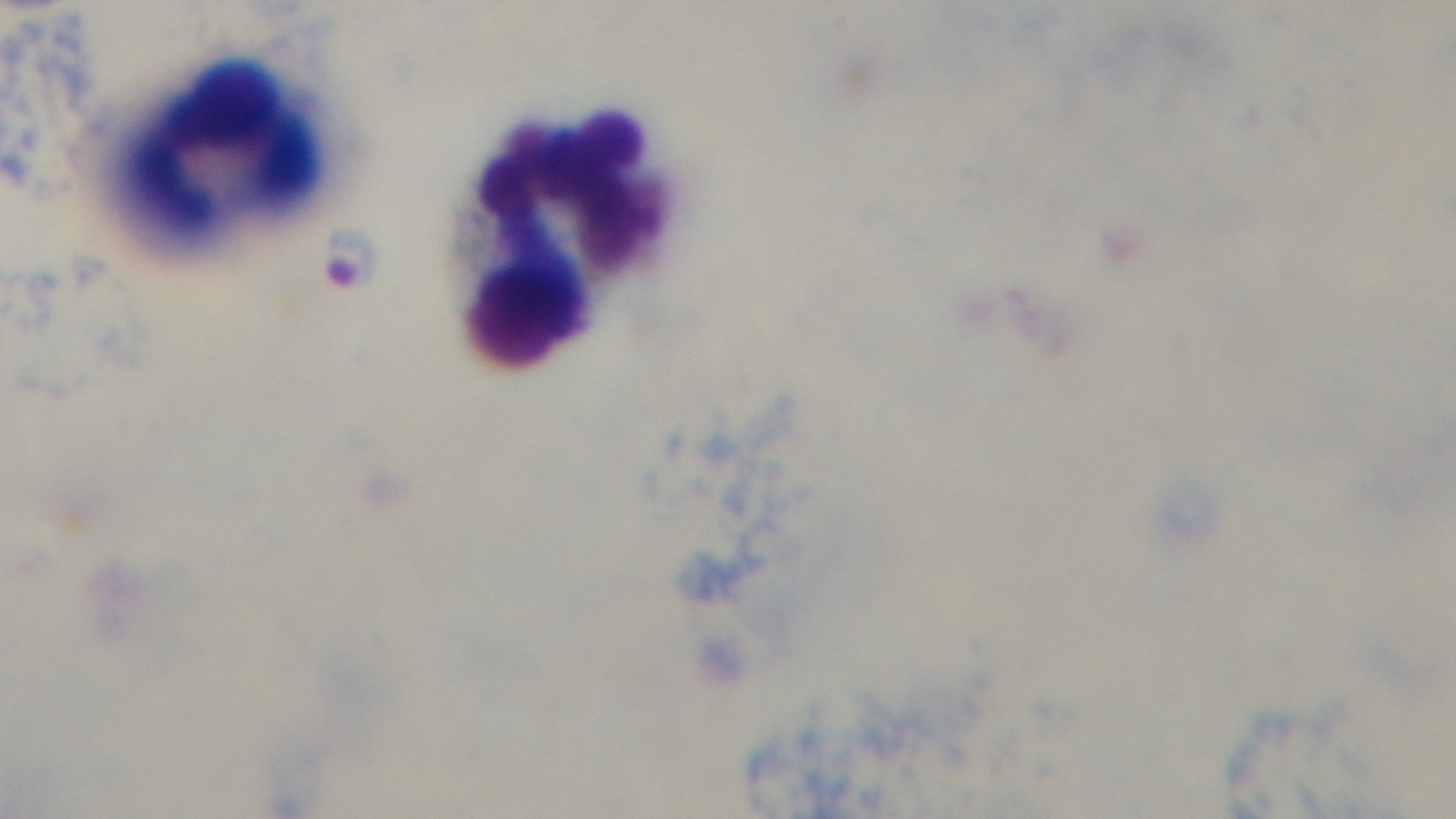 100x oil-immersion objective. Preparation: thick smear. Captured with a mounted 4K digital camera. Giemsa-stained. Malaria status: infected. Light microscopy. Single field of view.